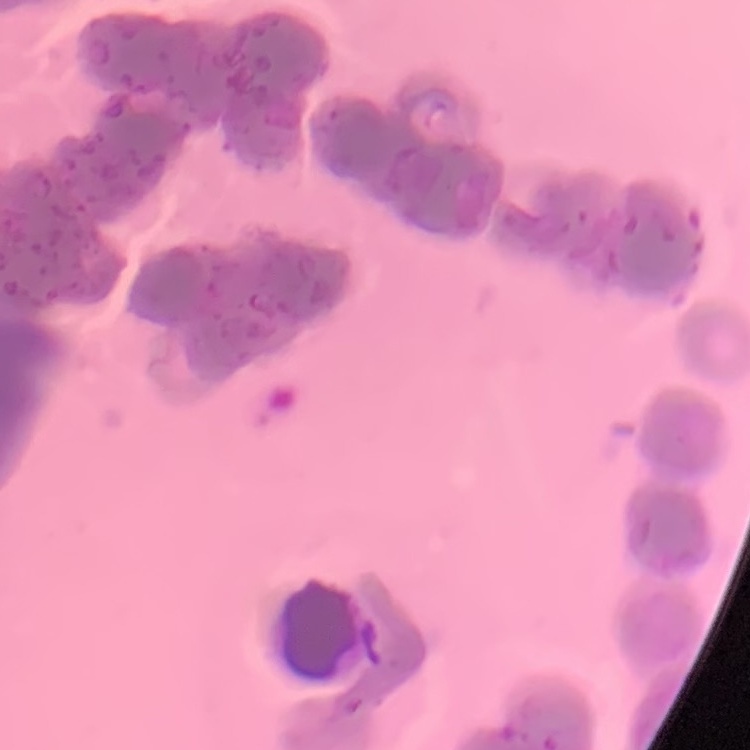

Summary:
  - Erythrocyte morphology: rouleaux formation
  - Image type: square crop of a larger photomicrograph
  - Stain: Field's or Giemsa
  - Preparation: thin peripheral smear